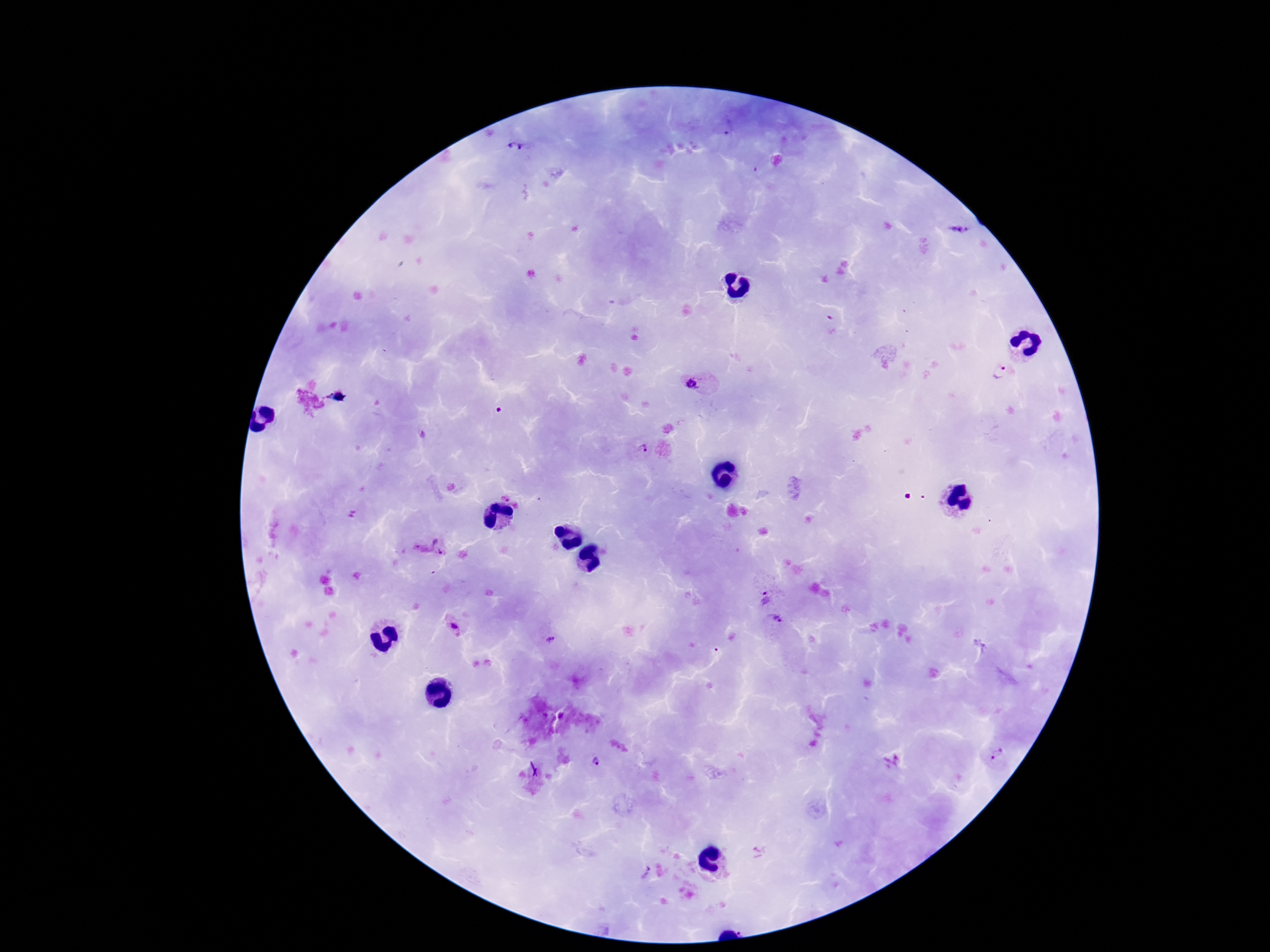
Approximate centers as {x, y} in pixels. Plasmodium parasite locations: {517, 148}, {959, 230}, {829, 323}, {1001, 373}, {693, 383}, {335, 397}, {641, 451}, {429, 547}, {764, 598}, {776, 619}, {456, 629}, {549, 639}, {996, 755}, {595, 762}, {644, 873}. Photographed through the microscope eyepiece with a smartphone camera. 100x magnification. Patient malaria status: infected. Giemsa stain. Thick blood film. Image is 1270×952 pixels. Single field of view.